Comment on the morphology of the red blood cells.
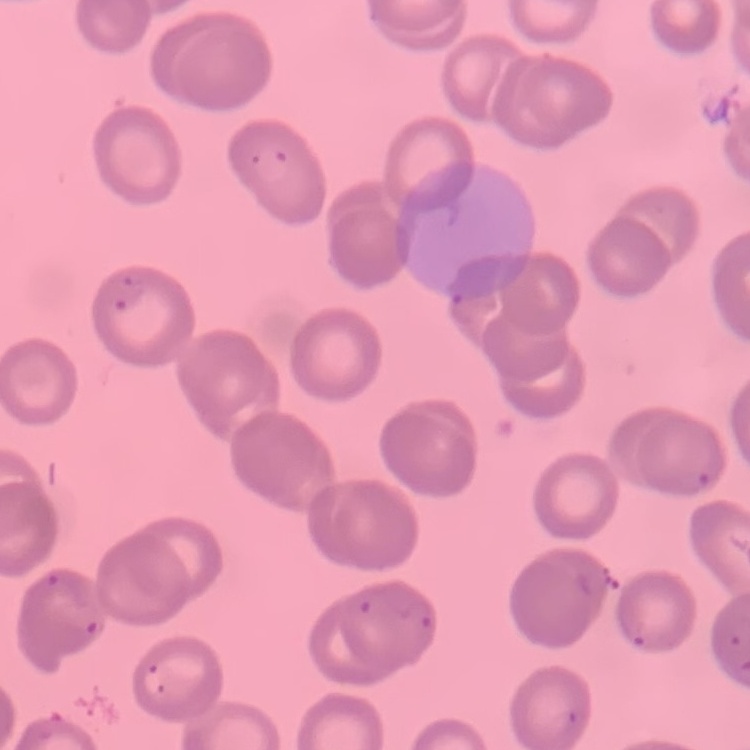
They show no rouleaux formation.

Stained with either Field's or Giemsa. One tile cut from a larger photomicrograph. Thin blood film.